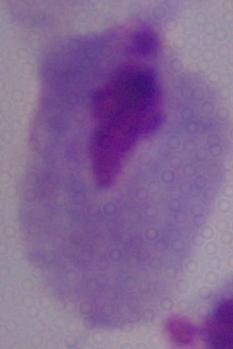
Summary:
  - Magnification: 1000x
  - Modality: photomicrograph
  - Identification: trichomonad